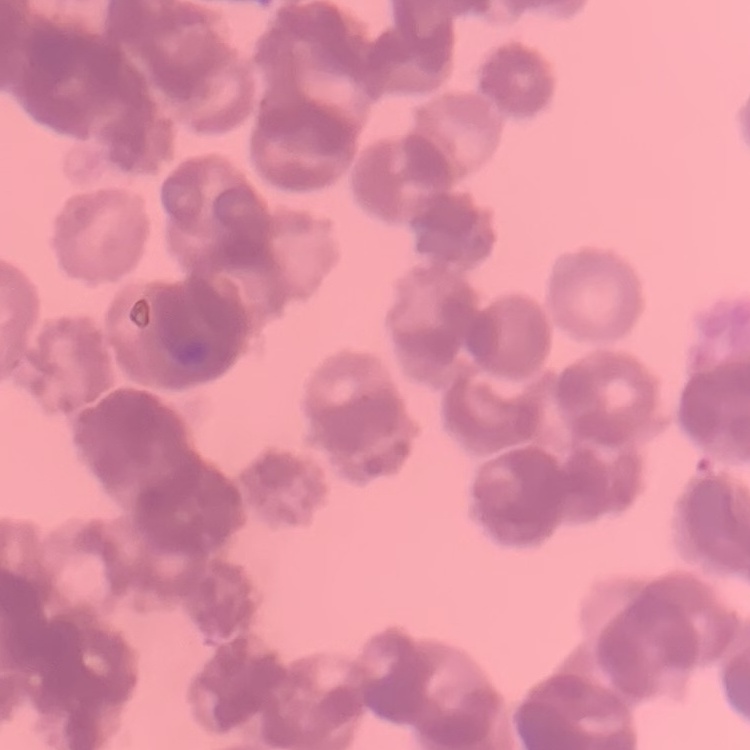

{
  "red_blood_cell_morphology": "rouleaux formation",
  "image_type": "square crop of a larger photomicrograph",
  "stain": "Field's or Giemsa",
  "preparation": "thin peripheral smear"
}